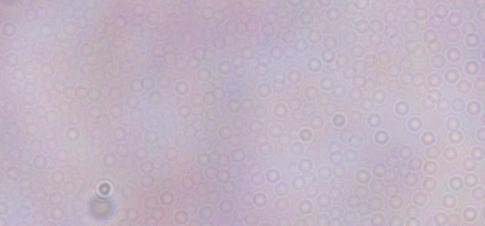
Summary:
  - Modality: photomicrograph
  - Magnification: 1000x
  - Identification: trypanosome